Locate and identify every blood parasite.
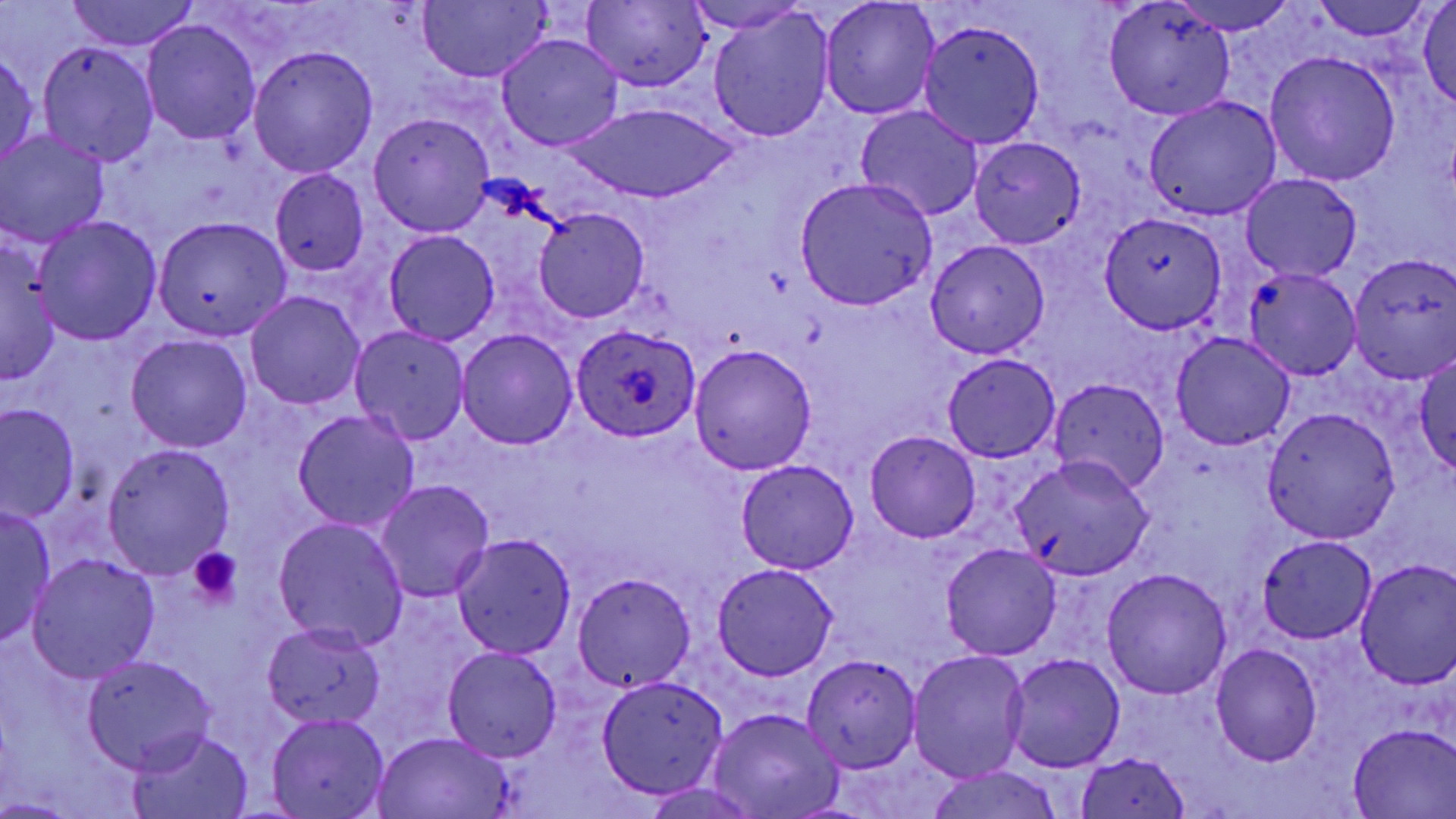

Approximate bounding boxes as named x1/y1/x2/y2 corners in pixels.
Plasmodium ovale-infected red blood cells: (x1=571, y1=322, x2=699, y2=442).
No Plasmodium falciparum, Plasmodium malariae, Plasmodium vivax, Babesia divergens, or Trypanosoma brucei observed.

{
  "slide_level_diagnosis": "Plasmodium ovale",
  "preparation": "thin blood smear",
  "field_of_view": "one of a larger specimen",
  "uninfected_red_blood_cell_locations": "approximate bounding boxes as named x1/y1/x2/y2 corners in pixels: (x1=63, y1=0, x2=203, y2=52), (x1=1169, y1=0, x2=1295, y2=33), (x1=415, y1=1, x2=551, y2=82), (x1=684, y1=1, x2=810, y2=35), (x1=818, y1=1, x2=941, y2=119), (x1=1315, y1=1, x2=1430, y2=40), (x1=581, y1=2, x2=710, y2=89), (x1=1417, y1=2, x2=1456, y2=107), (x1=1102, y1=3, x2=1235, y2=122), (x1=707, y1=9, x2=835, y2=142), (x1=142, y1=19, x2=261, y2=144), (x1=918, y1=21, x2=1044, y2=149), (x1=495, y1=32, x2=625, y2=152), (x1=139, y1=34, x2=374, y2=161), (x1=36, y1=42, x2=159, y2=166), (x1=248, y1=45, x2=379, y2=177), (x1=0, y1=46, x2=40, y2=171), (x1=1264, y1=50, x2=1401, y2=185), (x1=1143, y1=96, x2=1282, y2=222), (x1=570, y1=103, x2=727, y2=204), (x1=854, y1=106, x2=984, y2=222), (x1=368, y1=113, x2=494, y2=236), (x1=822, y1=122, x2=961, y2=272), (x1=0, y1=130, x2=109, y2=247), (x1=970, y1=137, x2=1086, y2=249), (x1=270, y1=170, x2=371, y2=276), (x1=1240, y1=174, x2=1361, y2=281), (x1=794, y1=177, x2=937, y2=308), (x1=534, y1=207, x2=649, y2=322), (x1=1099, y1=212, x2=1228, y2=334), (x1=33, y1=215, x2=161, y2=345), (x1=154, y1=215, x2=290, y2=342), (x1=383, y1=231, x2=499, y2=347), (x1=0, y1=234, x2=60, y2=387), (x1=925, y1=239, x2=1050, y2=360), (x1=1347, y1=252, x2=1456, y2=380), (x1=1244, y1=269, x2=1361, y2=380), (x1=245, y1=290, x2=367, y2=410), (x1=349, y1=326, x2=471, y2=444), (x1=456, y1=329, x2=578, y2=449), (x1=1171, y1=333, x2=1295, y2=452), (x1=124, y1=334, x2=253, y2=453), (x1=689, y1=344, x2=817, y2=474), (x1=1412, y1=353, x2=1456, y2=475), (x1=941, y1=355, x2=1062, y2=461), (x1=1049, y1=378, x2=1168, y2=496), (x1=1, y1=403, x2=80, y2=523), (x1=1262, y1=406, x2=1401, y2=543), (x1=292, y1=408, x2=419, y2=534), (x1=865, y1=429, x2=980, y2=541), (x1=101, y1=443, x2=234, y2=577), (x1=1010, y1=455, x2=1154, y2=581), (x1=736, y1=459, x2=859, y2=575), (x1=373, y1=480, x2=495, y2=603), (x1=296, y1=501, x2=489, y2=632), (x1=0, y1=505, x2=56, y2=649), (x1=271, y1=517, x2=410, y2=653), (x1=451, y1=534, x2=577, y2=659), (x1=1257, y1=535, x2=1378, y2=643), (x1=940, y1=544, x2=1063, y2=661), (x1=27, y1=554, x2=160, y2=682), (x1=1355, y1=559, x2=1456, y2=690), (x1=712, y1=563, x2=838, y2=681), (x1=1102, y1=568, x2=1232, y2=699), (x1=572, y1=572, x2=697, y2=692), (x1=262, y1=621, x2=387, y2=729), (x1=1210, y1=644, x2=1322, y2=766), (x1=442, y1=647, x2=563, y2=761), (x1=907, y1=649, x2=1030, y2=781), (x1=801, y1=653, x2=923, y2=774), (x1=1004, y1=653, x2=1125, y2=771), (x1=81, y1=654, x2=218, y2=772), (x1=595, y1=673, x2=730, y2=800), (x1=708, y1=708, x2=844, y2=819), (x1=265, y1=712, x2=391, y2=818), (x1=1348, y1=724, x2=1455, y2=818), (x1=124, y1=728, x2=254, y2=819), (x1=372, y1=730, x2=514, y2=818), (x1=1073, y1=750, x2=1193, y2=818), (x1=920, y1=766, x2=1066, y2=819), (x1=638, y1=783, x2=766, y2=819)",
  "magnification": "1000x",
  "stain": "May-Grünwald-Giemsa",
  "modality": "light microscopy",
  "platelet_locations": "approximate bounding boxes as named x1/y1/x2/y2 corners in pixels: (x1=186, y1=548, x2=241, y2=612)",
  "image_size": "1456×819 pixels"
}